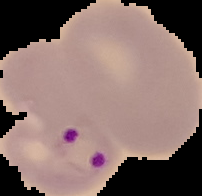
Summary:
  - Preparation: thin blood smear
  - Malaria status: parasitized
  - Image type: cell region segmented out of the field of view; surrounding area masked to black
  - Image size: 202×196 pixels